Give the extent of all Plasmodium falciparum-infected red blood cells.
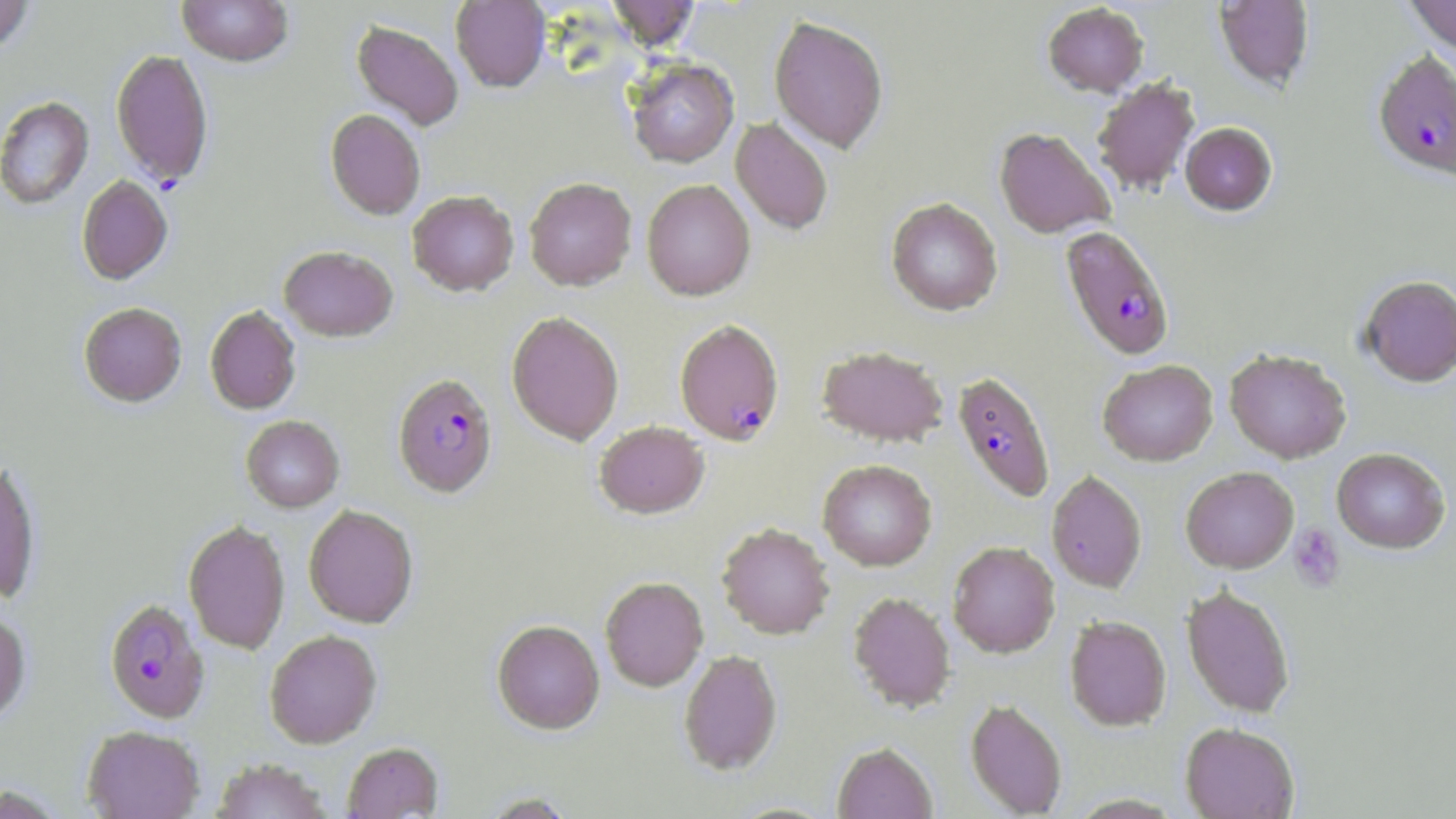

Approximate bounding boxes as (x1,y1)-(x2,y2) corner pairs in pixels.
Plasmodium falciparum-infected red blood cells: (1373,50)-(1455,180), (1060,225)-(1174,360), (674,319)-(784,446), (952,371)-(1055,502), (392,373)-(497,498), (104,599)-(209,723).

Platelet locations: (1288,523)-(1346,593). Uninfected red blood cell locations: (177,0)-(293,67), (451,0)-(550,93), (606,0)-(701,52), (1405,0)-(1456,55), (0,1)-(35,55), (1214,1)-(1314,91), (1043,3)-(1148,97), (769,16)-(888,153), (351,20)-(464,131), (111,48)-(214,186), (627,59)-(739,168), (1092,79)-(1200,196), (0,96)-(93,210), (325,109)-(425,220), (731,118)-(833,235), (1180,122)-(1277,215), (994,128)-(1115,239), (77,175)-(173,286), (524,178)-(636,290), (642,179)-(755,301), (407,191)-(519,297), (886,197)-(1003,315), (279,246)-(398,342), (1359,275)-(1456,386), (79,302)-(187,407), (205,306)-(301,414), (506,311)-(624,445), (817,345)-(948,447), (1224,348)-(1351,463), (1098,360)-(1217,466), (241,415)-(344,512), (595,421)-(709,519), (1332,448)-(1450,553), (0,459)-(41,605), (818,459)-(937,571), (1181,466)-(1298,573), (1046,470)-(1147,592), (304,505)-(418,628), (183,520)-(290,655), (716,523)-(834,639), (948,541)-(1060,657), (599,577)-(708,692), (1182,585)-(1295,718), (848,592)-(956,713), (0,610)-(31,725), (1065,615)-(1171,731), (492,620)-(605,735), (264,630)-(382,748), (679,650)-(782,775), (965,698)-(1067,817), (1181,722)-(1299,818), (82,726)-(205,819), (342,742)-(442,818), (832,742)-(937,819), (211,759)-(331,819), (1,784)-(67,818), (479,792)-(579,818). Slide-level diagnosis: Plasmodium falciparum. Image is 1456×819 pixels. May-Grünwald-Giemsa stain. 1000x magnification. Light microscopy. Thin blood film. Single field of view.